Identify the parasite.
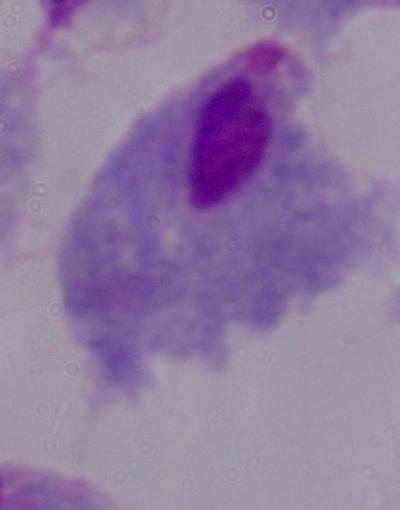
This is a trichomonad.

Summary:
  - Magnification: 1000x
  - Modality: photomicrograph